Locate every Plasmodium falciparum-infected red blood cell.
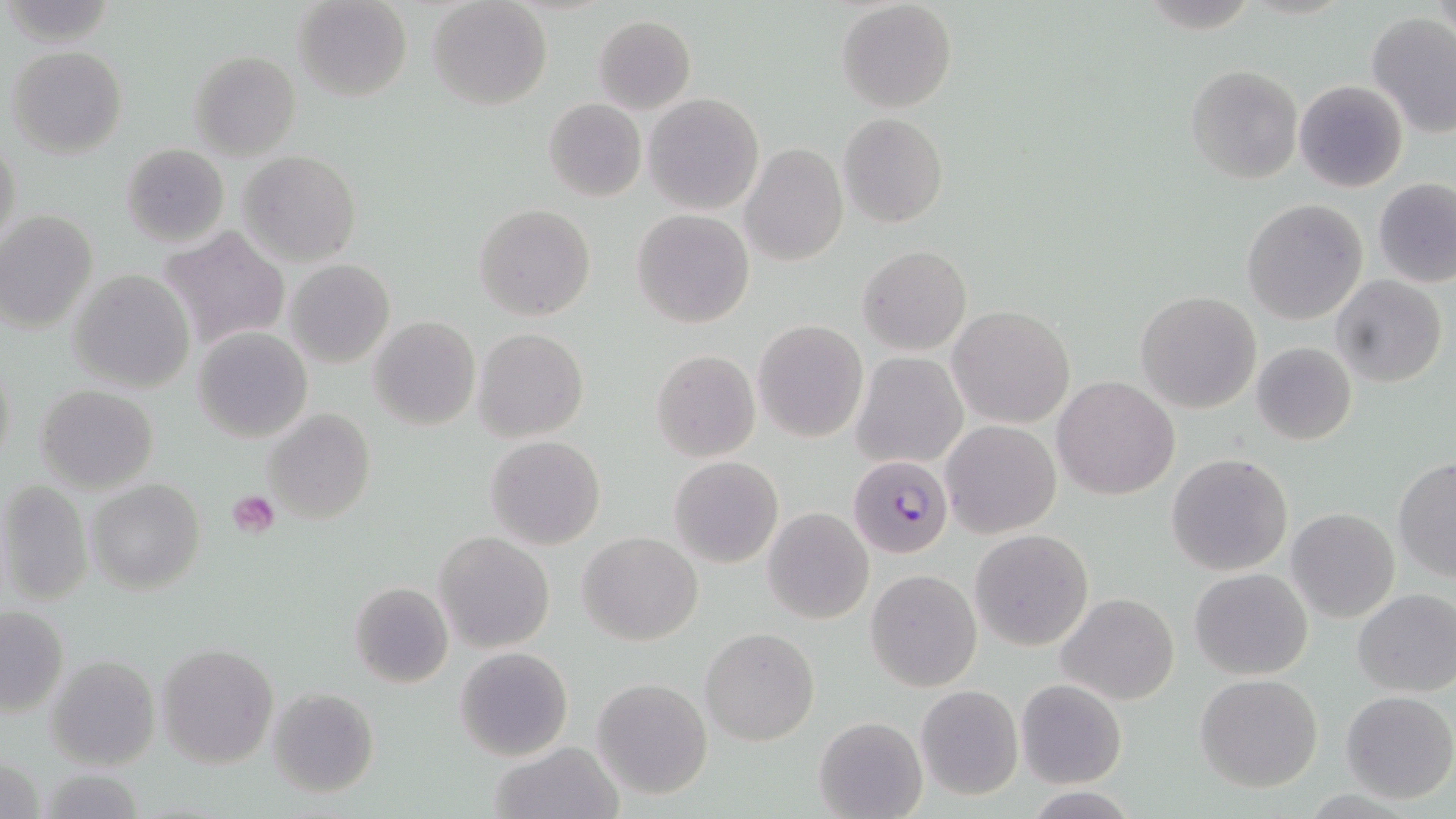
Approximate bounding boxes as [x1, y1, x2, y2] in pixels.
Plasmodium falciparum-infected red blood cells: [849, 455, 954, 558].

Summary:
  - Uninfected red blood cell locations: [292, 0, 412, 102], [428, 0, 551, 109], [835, 1, 957, 114], [1366, 12, 1456, 138], [592, 15, 696, 114], [7, 45, 127, 158], [190, 50, 300, 160], [1186, 65, 1303, 184], [1295, 79, 1408, 192], [643, 92, 764, 214], [543, 98, 646, 201], [837, 112, 949, 229], [1, 137, 23, 253], [121, 143, 229, 247], [740, 143, 848, 266], [239, 150, 361, 265], [1373, 179, 1456, 287], [1242, 198, 1368, 325], [475, 203, 596, 321], [632, 208, 754, 328], [0, 210, 97, 333], [159, 225, 290, 353], [858, 245, 972, 355], [287, 258, 394, 367], [68, 270, 195, 394], [1332, 276, 1447, 387], [1135, 290, 1263, 413], [947, 305, 1076, 428], [369, 317, 480, 432], [753, 319, 867, 442], [192, 328, 313, 442], [473, 328, 589, 444], [1250, 342, 1358, 445], [651, 350, 759, 461], [850, 351, 968, 470], [1, 354, 15, 475], [1053, 375, 1178, 499], [35, 385, 158, 493], [264, 409, 375, 527], [941, 419, 1061, 538], [484, 436, 606, 551], [1166, 453, 1294, 576], [669, 456, 783, 569], [1393, 456, 1456, 581], [86, 478, 205, 594], [1, 480, 93, 605], [761, 507, 875, 625], [1286, 508, 1400, 623], [970, 530, 1093, 651], [434, 531, 554, 653], [578, 531, 703, 646], [1189, 568, 1312, 679], [867, 569, 981, 691], [349, 581, 454, 689], [1353, 588, 1456, 697], [1057, 593, 1180, 706], [0, 606, 68, 715], [700, 628, 820, 746], [158, 642, 279, 769], [454, 647, 574, 762], [46, 655, 159, 769], [1195, 674, 1323, 792], [592, 677, 713, 802], [1015, 680, 1126, 787], [916, 686, 1022, 799], [267, 687, 379, 798], [1339, 690, 1455, 804], [813, 716, 927, 819], [490, 741, 622, 819]
  - Platelet locations: [228, 491, 281, 537]
  - Slide-level diagnosis: Plasmodium falciparum
  - Preparation: thin blood smear
  - Stain: May-Grünwald-Giemsa
  - Field of view: one of a larger specimen
  - Modality: optical microscopy
  - Image size: 1456×819 pixels
  - Magnification: 1000x